Classify this cell by malaria status.
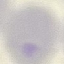

It is uninfected.

Thin blood film. Acquired by smartphone through the microscope eyepiece. Automatically extracted cell patch, resized to 64 × 64 pixels. Giemsa stain.